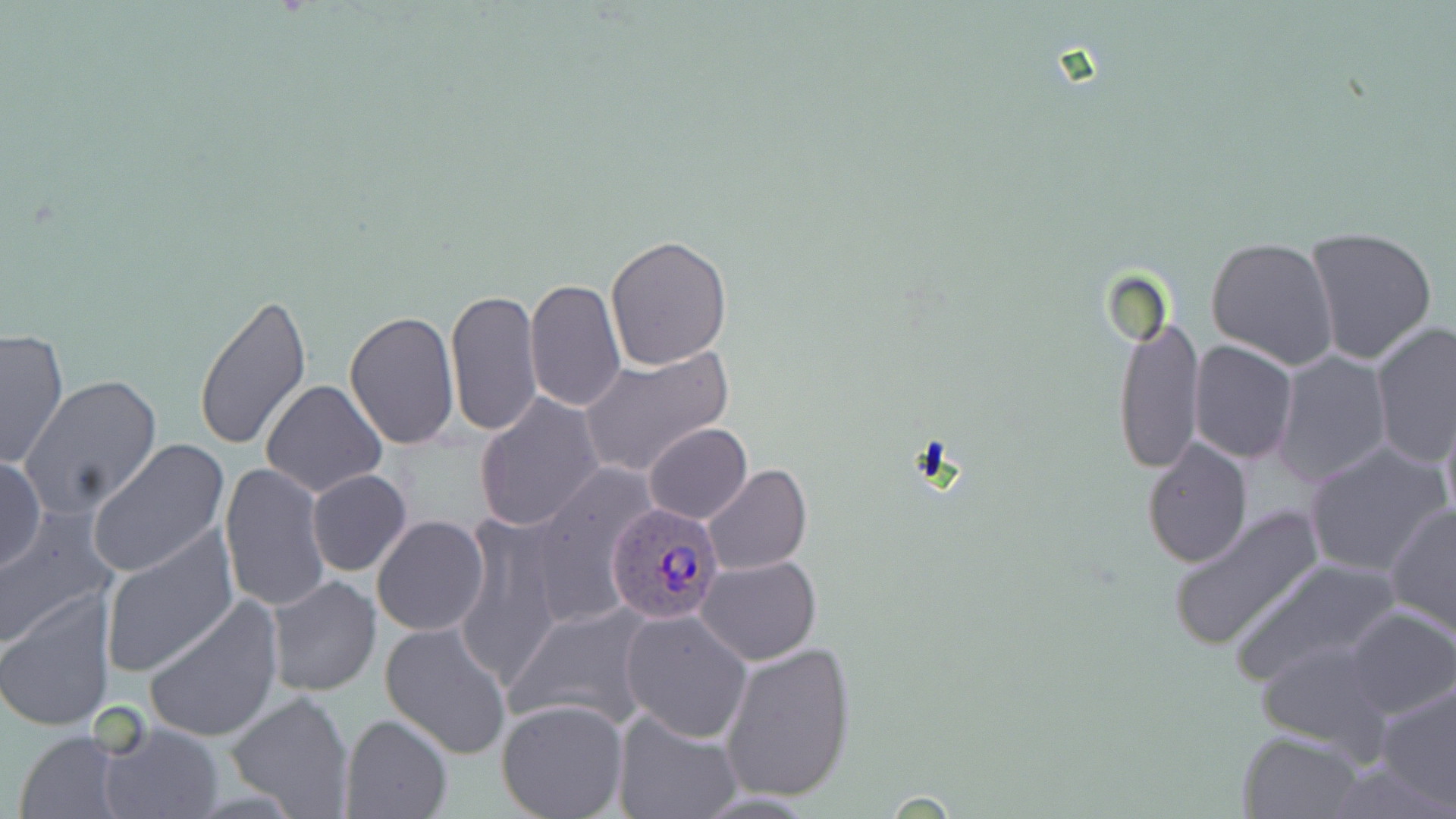
Approximate bounding boxes as (x1,y1)-(x2,y2) corner pairs in pixels. Uninfected red blood cell locations: (1304,226)-(1437,364), (605,236)-(733,370), (1206,238)-(1339,370), (525,277)-(625,413), (445,287)-(544,438), (192,290)-(310,452), (345,307)-(460,451), (1111,313)-(1204,474), (1369,321)-(1455,472), (1,327)-(69,469), (1189,340)-(1298,465), (581,346)-(734,479), (1273,350)-(1392,489), (24,374)-(163,515), (260,380)-(386,499), (474,393)-(606,534), (1438,399)-(1456,530), (644,424)-(750,522), (1141,438)-(1252,570), (86,439)-(229,579), (1302,441)-(1450,579), (0,453)-(45,577), (219,462)-(330,613), (521,462)-(659,633), (702,464)-(811,576), (306,469)-(412,578), (1384,501)-(1456,639), (1168,504)-(1326,655), (0,512)-(117,647), (449,515)-(567,687), (372,516)-(490,637), (99,528)-(240,680), (696,554)-(822,665), (1230,555)-(1400,689), (267,575)-(380,697), (1,590)-(117,733), (144,598)-(283,744), (505,602)-(657,734), (1344,607)-(1456,719), (619,608)-(752,742), (379,620)-(513,760), (1256,638)-(1396,754), (718,639)-(857,802), (1375,680)-(1456,811), (226,691)-(355,817), (496,697)-(630,818), (613,709)-(743,819), (339,714)-(452,819), (100,722)-(223,819), (13,730)-(124,819), (1238,730)-(1365,818). Plasmodium ovale-infected red blood cell locations: (603,500)-(722,625). Slide-level diagnosis: Plasmodium ovale. Image is 1456×819 pixels. One field of a larger specimen. Optical microscopy. May-Grünwald-Giemsa stain. Captured at 1000x magnification. Thin blood film.